Describe the morphology of the red blood cells.
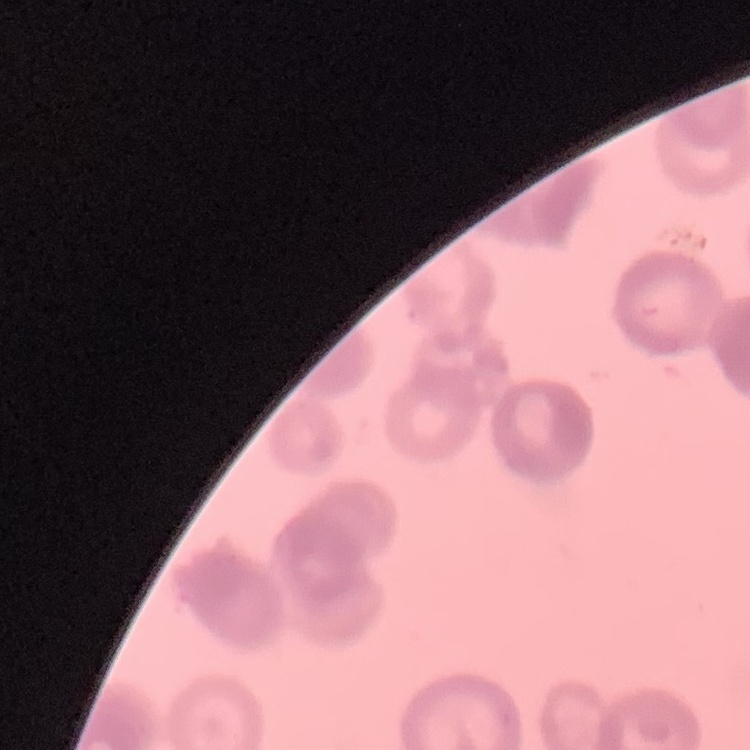

They show rouleaux formation.

image type = square crop of a larger photomicrograph
stain = Field's or Giemsa
preparation = thin blood smear